Locate every uninfected red blood cell.
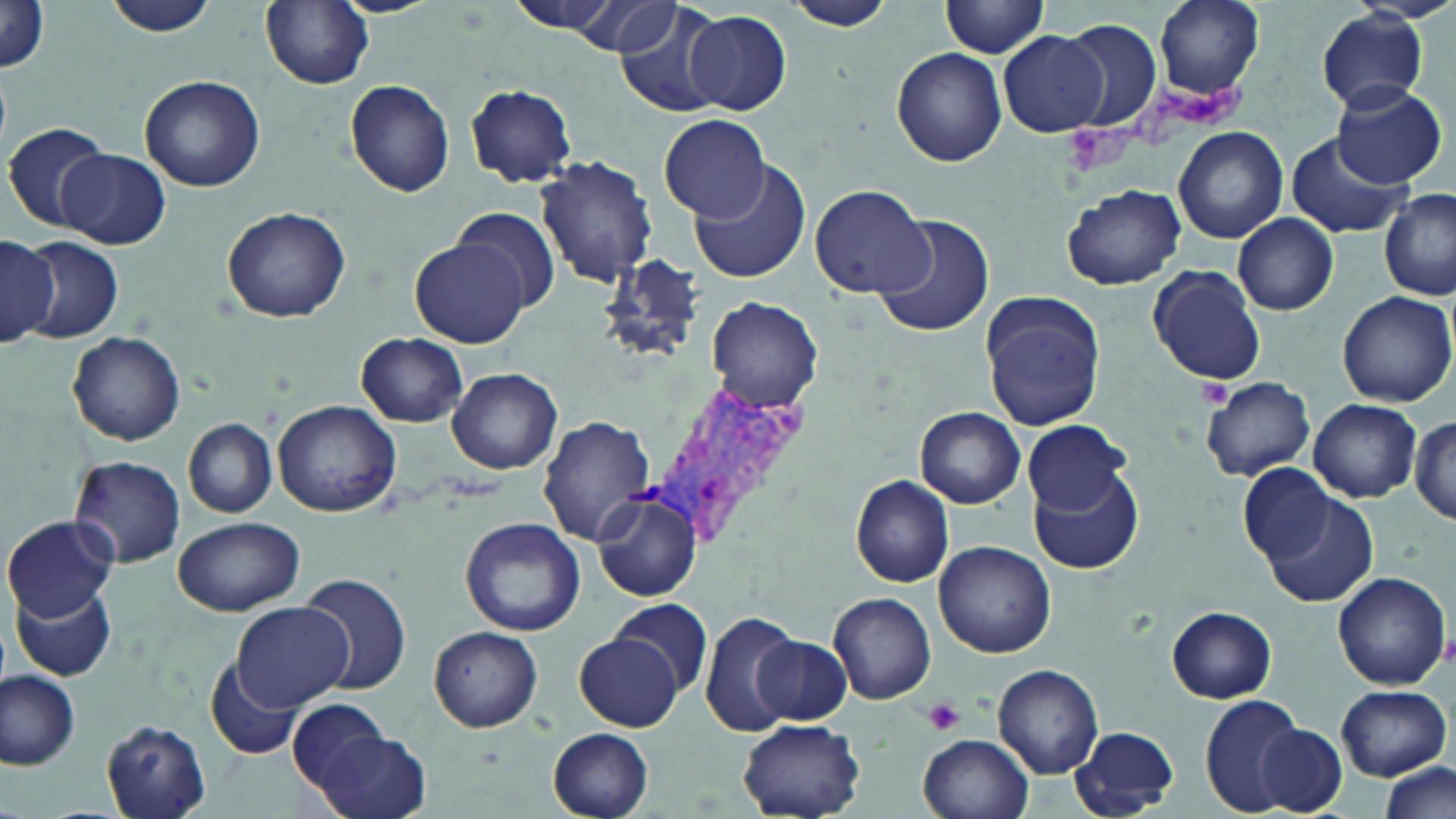

Approximate bounding boxes as (x1,y1)-(x2,y2) corner pairs in pixels.
Uninfected red blood cells: (102,0)-(221,39), (502,0)-(627,37), (577,0)-(680,55), (611,0)-(731,116), (1152,0)-(1263,99), (260,1)-(374,88), (781,1)-(902,31), (941,1)-(1052,57), (1,4)-(51,75), (684,9)-(791,116), (1317,9)-(1430,111), (1056,18)-(1163,132), (998,30)-(1107,138), (891,47)-(1008,167), (140,74)-(265,192), (345,80)-(456,198), (1332,82)-(1447,189), (463,83)-(578,187), (660,114)-(769,221), (4,122)-(111,233), (1173,126)-(1287,244), (1284,132)-(1412,242), (59,149)-(170,249), (534,155)-(657,287), (691,163)-(811,285), (808,182)-(931,299), (1063,184)-(1186,290), (1380,189)-(1456,300), (451,206)-(562,314), (222,207)-(351,323), (870,212)-(995,340), (1233,212)-(1339,315), (0,234)-(58,348), (22,236)-(122,343), (412,239)-(531,348), (1147,264)-(1268,386), (1338,290)-(1453,407), (981,291)-(1107,430), (705,295)-(825,410), (67,330)-(186,446), (355,334)-(469,426), (447,367)-(563,474), (1202,377)-(1314,480), (272,399)-(401,517), (1309,399)-(1420,502), (916,406)-(1026,508), (1411,414)-(1455,524), (540,415)-(657,545), (184,417)-(277,518), (1023,419)-(1130,515), (69,455)-(186,568), (1240,463)-(1333,560), (1032,466)-(1144,574), (850,475)-(955,587), (591,491)-(703,602), (1260,491)-(1378,607), (3,515)-(117,620), (172,516)-(304,615), (460,517)-(586,637), (933,542)-(1056,657), (1332,571)-(1450,689), (300,573)-(411,697), (12,582)-(117,681), (828,592)-(935,706), (613,596)-(712,696), (230,602)-(354,713), (1167,607)-(1277,703), (698,611)-(803,735), (427,626)-(543,732), (575,631)-(683,730), (754,635)-(851,725), (206,656)-(307,760), (993,664)-(1104,776), (0,668)-(80,770), (1336,684)-(1451,780), (288,695)-(392,796), (1199,695)-(1310,815), (100,720)-(213,819), (737,720)-(865,818), (1257,724)-(1349,813), (1068,725)-(1182,817), (548,728)-(654,819), (312,731)-(432,819), (919,733)-(1034,819), (1377,759)-(1453,818).

Summary:
  - Platelet locations: (1158,85)-(1250,129), (1063,123)-(1137,177), (1194,379)-(1235,408), (922,696)-(965,735)
  - Plasmodium vivax-infected red blood cell locations: (648,376)-(804,554)
  - Slide-level diagnosis: Plasmodium vivax
  - Stain: May-Grünwald-Giemsa
  - Magnification: 1000x
  - Modality: optical microscopy
  - Image size: 1456×819 pixels
  - Preparation: thin blood film
  - Field of view: one of a larger specimen